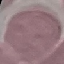
Summary:
  - Malaria status: uninfected
  - Capture: smartphone camera at the microscope eyepiece
  - Stain: Giemsa
  - Image type: automatically extracted cell patch, resized to 64 × 64 pixels
  - Preparation: thin blood film